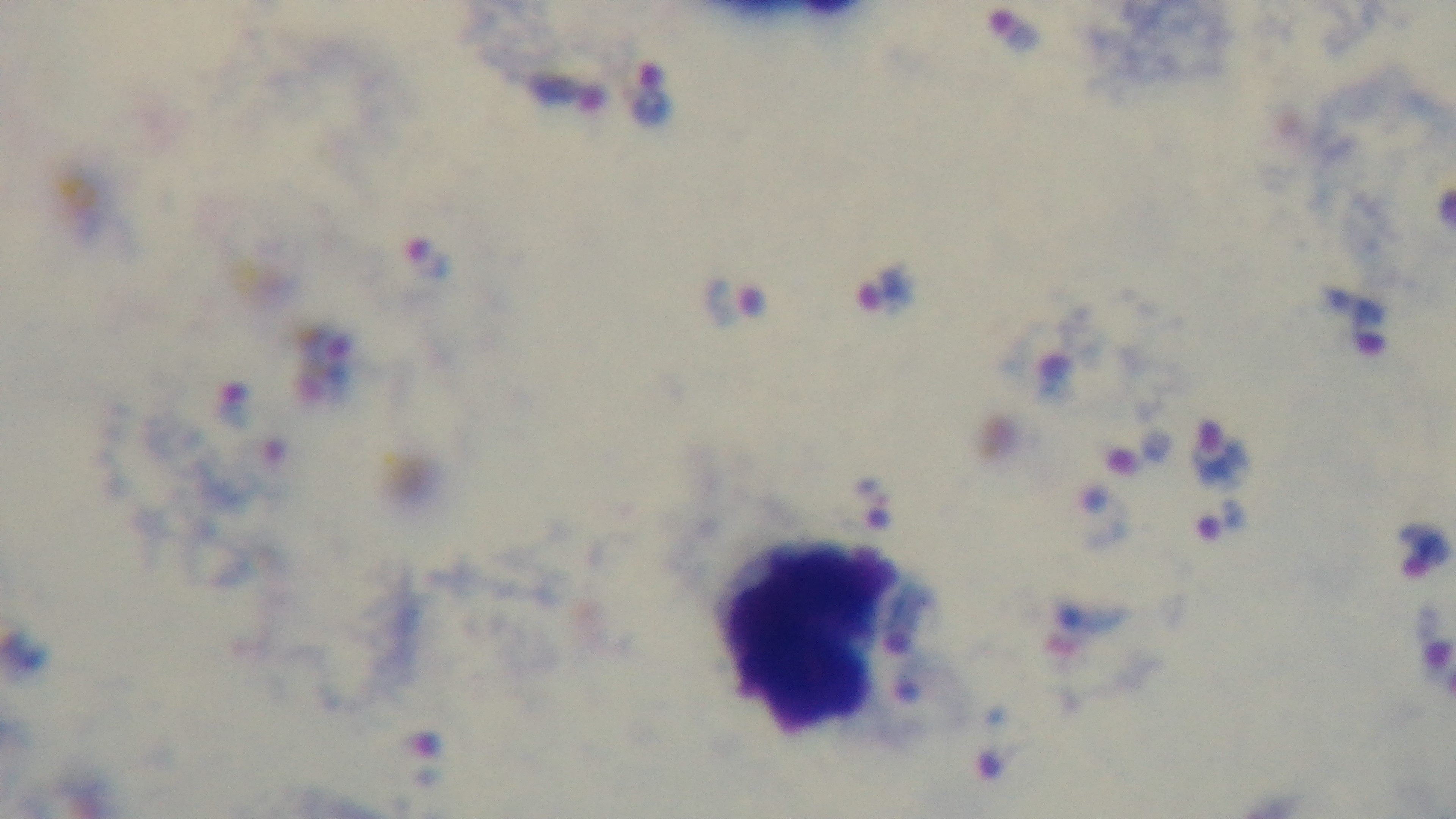
Giemsa-stained. Preparation: thick blood film. Photomicrograph. One field from the slide. Oil-immersion objective, 100x. Captured with a mounted 4K digital camera. Malaria status: positive.